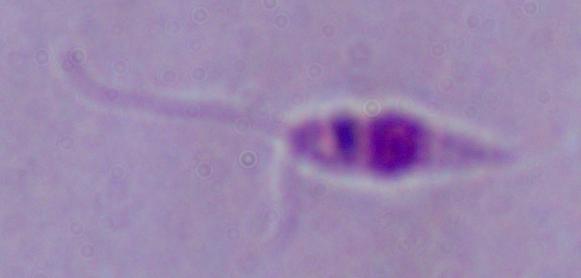

Summary:
  - Magnification: 1000x
  - Identification: Leishmania
  - Modality: photomicrograph